Locate every blood parasite and identify its species.
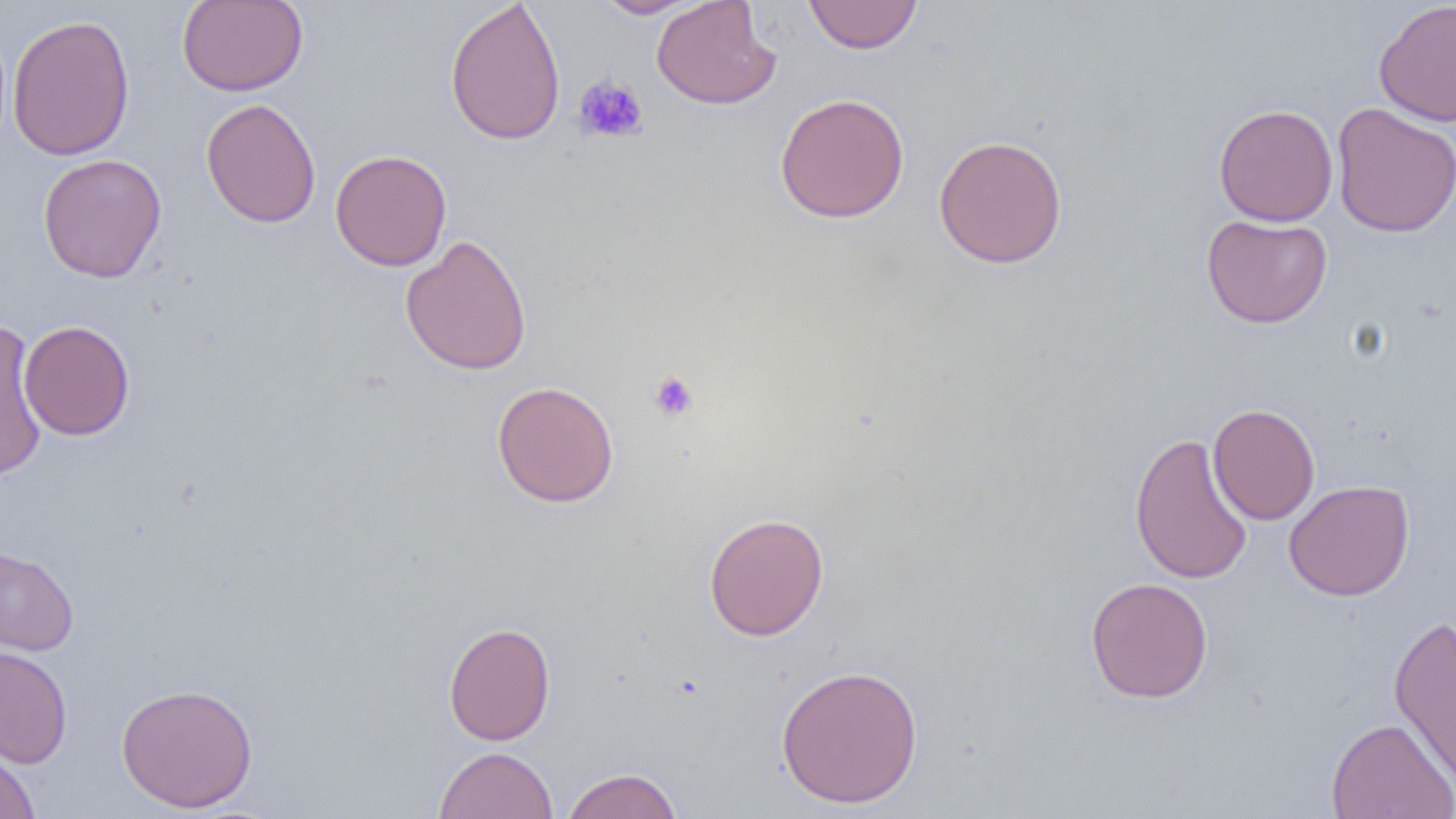

No blood parasites seen.

Summary:
  - Coordinate format: approximate bounding boxes as (x1,y1)-(x2,y2) corner pairs in pixels
  - Platelet locations: (573,75)-(649,144), (648,370)-(700,422)
  - Uninfected red blood cell locations: (176,0)-(308,97), (445,0)-(566,147), (594,0)-(701,18), (651,0)-(780,110), (803,0)-(923,54), (1373,1)-(1456,127), (6,13)-(135,161), (774,93)-(909,223), (201,98)-(321,228), (1214,103)-(1338,227), (1331,103)-(1456,238), (933,134)-(1068,269), (330,149)-(451,271), (37,153)-(167,283), (1201,213)-(1333,329), (400,234)-(532,376), (0,319)-(46,484), (18,320)-(135,441), (492,380)-(619,508), (1208,403)-(1320,525), (1129,432)-(1253,585), (1283,479)-(1415,601), (703,513)-(829,641), (0,544)-(79,655), (1085,576)-(1213,704), (1388,613)-(1456,791), (443,621)-(556,746), (0,646)-(73,768), (775,664)-(924,809), (116,681)-(258,813), (1326,716)-(1456,819), (0,746)-(41,819), (434,746)-(558,819), (561,767)-(683,819)
  - Slide-level diagnosis: negative for blood parasites
  - Preparation: thin blood film
  - Image size: 1456×819 pixels
  - Magnification: 1000x
  - Field of view: one of a larger specimen
  - Modality: optical microscopy